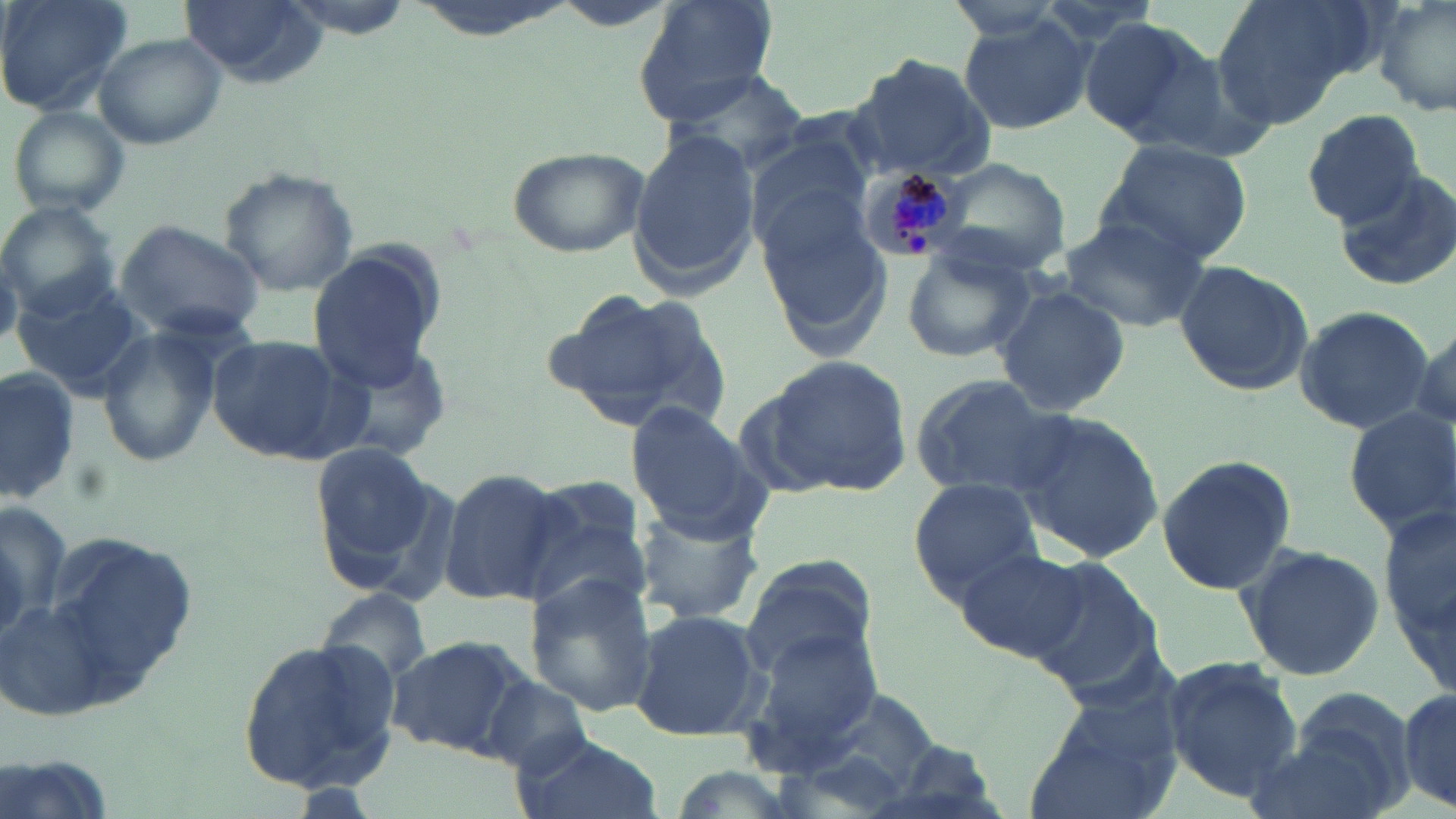
Summary:
  - Coordinate format: approximate bounding boxes as (x1,y1)-(x2,y2) corner pairs in pixels
  - Uninfected red blood cell locations: (0,0)-(134,117), (178,0)-(329,84), (638,0)-(779,113), (1209,0)-(1389,132), (1372,0)-(1455,118), (281,3)-(415,38), (956,14)-(1094,135), (1075,15)-(1218,143), (95,33)-(229,148), (843,54)-(997,183), (666,70)-(811,176), (7,103)-(132,219), (1302,109)-(1426,225), (742,120)-(879,249), (627,125)-(761,296), (1099,138)-(1252,268), (506,144)-(649,257), (921,153)-(1073,279), (219,166)-(358,296), (1332,166)-(1456,294), (756,188)-(893,356), (0,201)-(121,321), (1058,213)-(1210,332), (114,219)-(265,343), (307,244)-(445,392), (899,247)-(1038,366), (1172,260)-(1315,396), (8,275)-(151,398), (989,284)-(1131,418), (545,286)-(736,436), (1292,305)-(1434,432), (1409,317)-(1455,435), (96,326)-(220,467), (205,335)-(361,464), (762,355)-(913,497), (0,367)-(81,505), (910,375)-(1070,500), (624,401)-(769,541), (1342,406)-(1456,537), (1008,408)-(1164,563), (309,441)-(442,576), (1154,453)-(1297,596), (437,466)-(569,609), (519,478)-(655,610), (909,478)-(1043,601), (1380,497)-(1456,696), (630,502)-(765,626), (37,531)-(203,701), (951,544)-(1092,664), (1235,544)-(1385,683), (735,554)-(878,687), (1024,556)-(1162,693), (523,576)-(659,716), (315,587)-(436,689), (628,608)-(766,742), (740,630)-(886,769), (234,634)-(404,795), (384,634)-(531,757), (1162,656)-(1304,800), (478,674)-(593,774), (774,676)-(953,812), (1398,682)-(1453,813), (1022,692)-(1185,819), (1257,701)-(1414,819), (510,731)-(660,819), (0,749)-(117,819)
  - Plasmodium malariae-infected red blood cell locations: (857,164)-(965,258)
  - Slide-level diagnosis: Plasmodium malariae
  - Magnification: 1000x
  - Field of view: one of a larger specimen
  - Modality: light microscopy
  - Preparation: thin blood smear
  - Image size: 1456×819 pixels
  - Stain: May-Grünwald-Giemsa